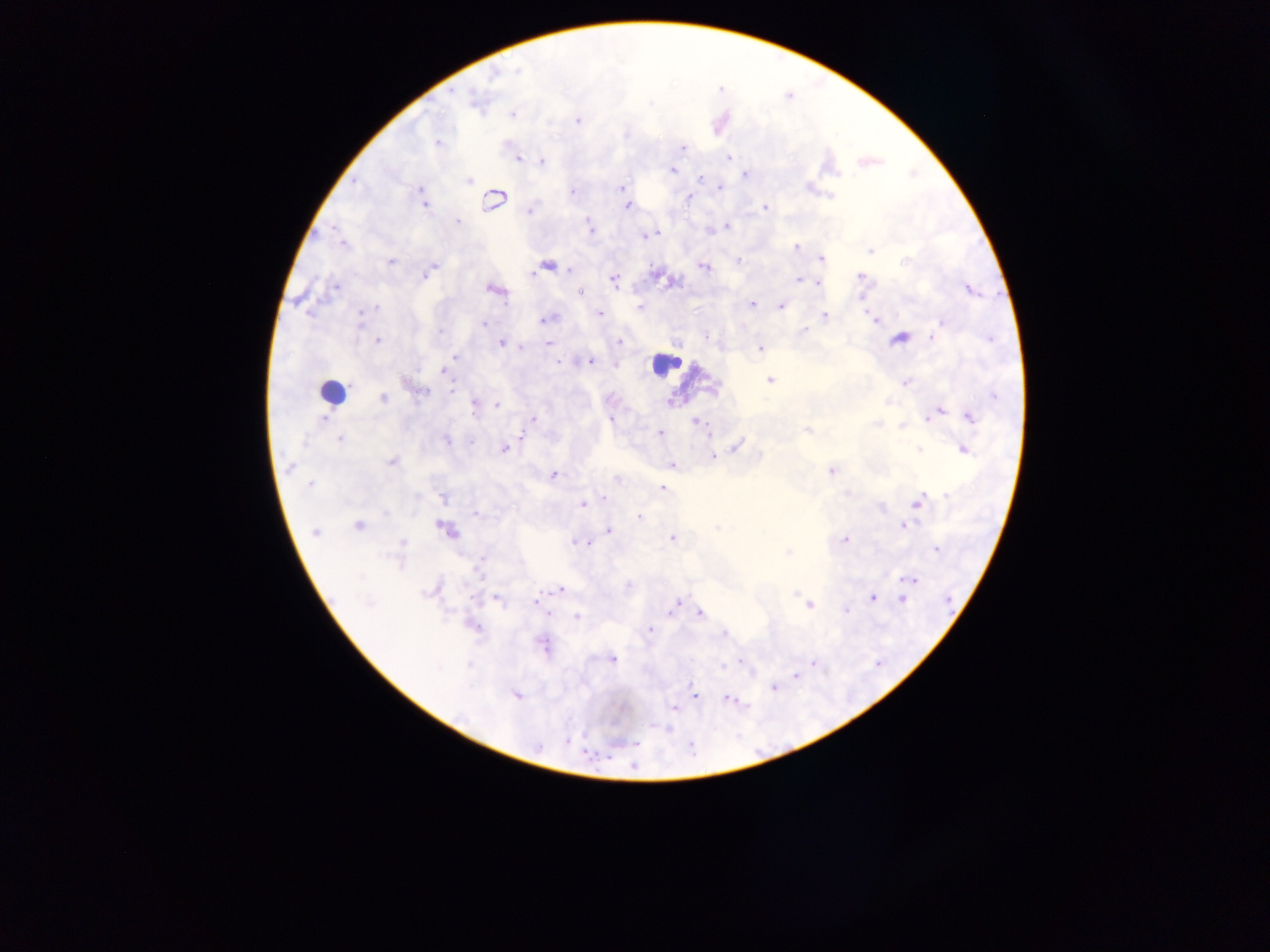 Approximate centers as {x, y} in pixels. Malaria parasite locations: {519, 68}, {492, 78}, {474, 104}, {511, 115}, {433, 116}, {577, 121}, {626, 134}, {437, 141}, {682, 148}, {518, 158}, {728, 158}, {542, 161}, {673, 170}, {744, 173}, {700, 177}, {468, 179}, {352, 182}, {623, 187}, {719, 187}, {419, 188}, {810, 188}, {571, 191}, {831, 196}, {687, 198}, {493, 201}, {425, 203}, {627, 207}, {766, 207}, {529, 211}, {457, 222}, {589, 222}, {591, 226}, {727, 228}, {711, 231}, {654, 233}, {644, 235}, {340, 241}, {798, 247}, {869, 250}, {739, 258}, {821, 259}, {391, 261}, {548, 266}, {703, 266}, {429, 271}, {861, 275}, {613, 280}, {799, 281}, {819, 282}, {972, 287}, {494, 290}, {580, 292}, {313, 295}, {324, 295}, {861, 295}, {297, 300}, {752, 304}, {638, 306}, {782, 307}, {376, 308}, {599, 314}, {360, 315}, {825, 316}, {545, 319}, {875, 321}, {483, 324}, {940, 325}, {802, 329}, {935, 334}, {990, 339}, {377, 340}, {620, 342}, {501, 343}, {549, 344}, {760, 347}, {455, 357}, {560, 361}, {592, 361}, {444, 371}, {769, 379}, {905, 383}, {451, 389}, {419, 395}, {994, 395}, {383, 398}, {670, 402}, {887, 403}, {497, 405}, {474, 408}, {940, 412}, {535, 417}, {969, 417}, {611, 418}, {322, 420}, {694, 423}, {876, 425}, {902, 426}, {806, 430}, {659, 433}, {711, 435}, {523, 436}, {337, 439}, {446, 439}, {743, 439}, {301, 443}, {738, 446}, {918, 449}, {504, 450}, {963, 450}, {714, 456}, {392, 462}, {671, 465}, {290, 469}, {831, 471}, {553, 474}, {310, 484}, {662, 489}, {846, 492}, {946, 495}, {605, 498}, {444, 499}, {916, 503}, {582, 504}, {882, 509}, {385, 513}, {477, 513}, {640, 519}, {357, 526}, {903, 526}, {445, 528}, {609, 530}, {315, 532}, {671, 537}, {846, 539}, {574, 542}, {589, 542}, {403, 543}, {581, 543}, {788, 551}, {935, 552}, {480, 564}, {399, 567}, {479, 572}, {361, 577}, {913, 580}, {559, 590}, {428, 591}, {795, 594}, {872, 597}, {474, 600}, {498, 600}, {535, 600}, {903, 601}, {677, 603}, {369, 604}, {812, 605}, {845, 610}, {701, 614}, {547, 615}, {576, 615}, {476, 628}, {650, 630}, {542, 643}, {612, 660}, {738, 663}, {813, 663}, {722, 664}, {795, 677}, {772, 688}, {695, 694}, {516, 697}, {727, 700}, {674, 709}. Leukocyte locations: {665, 363}, {336, 392}. Photographed through a microscope with a mobile-phone camera. Image is 1270×952 pixels. One field of view. Thick blood smear. Collected in Ghana.